Identify the parasite.
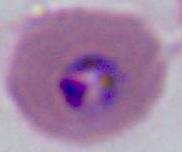

Plasmodium.

Summary:
  - Magnification: 400x or 1000x
  - Modality: micrograph